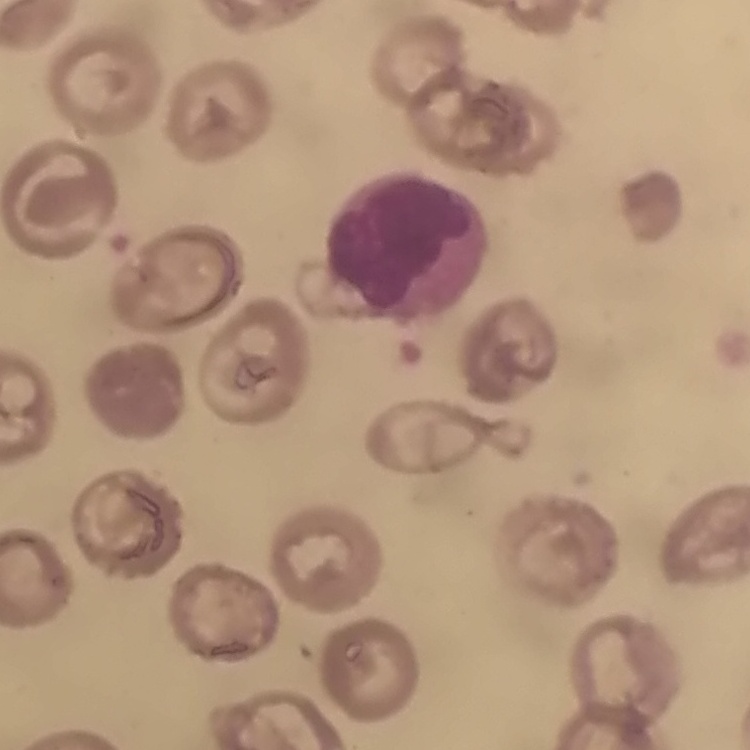

Summary:
  - Erythrocyte morphology: no rouleaux formation
  - Stain: Field's or Giemsa
  - Image type: square crop of a larger photomicrograph
  - Preparation: thin blood smear